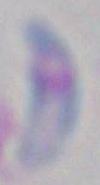

{
  "modality": "micrograph",
  "identification": "Toxoplasma gondii",
  "magnification": "1000x"
}